Name the parasite shown.
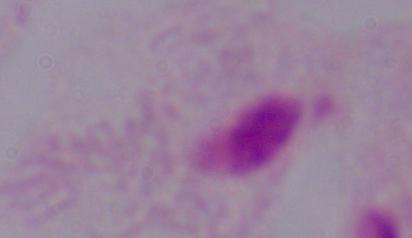

A trichomonad.

modality = micrograph
magnification = 1000x